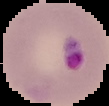
image type = segmented cell region with the area outside set to black
result = Plasmodium parasites detected
image size = 109×106 pixels
preparation = thin blood smear